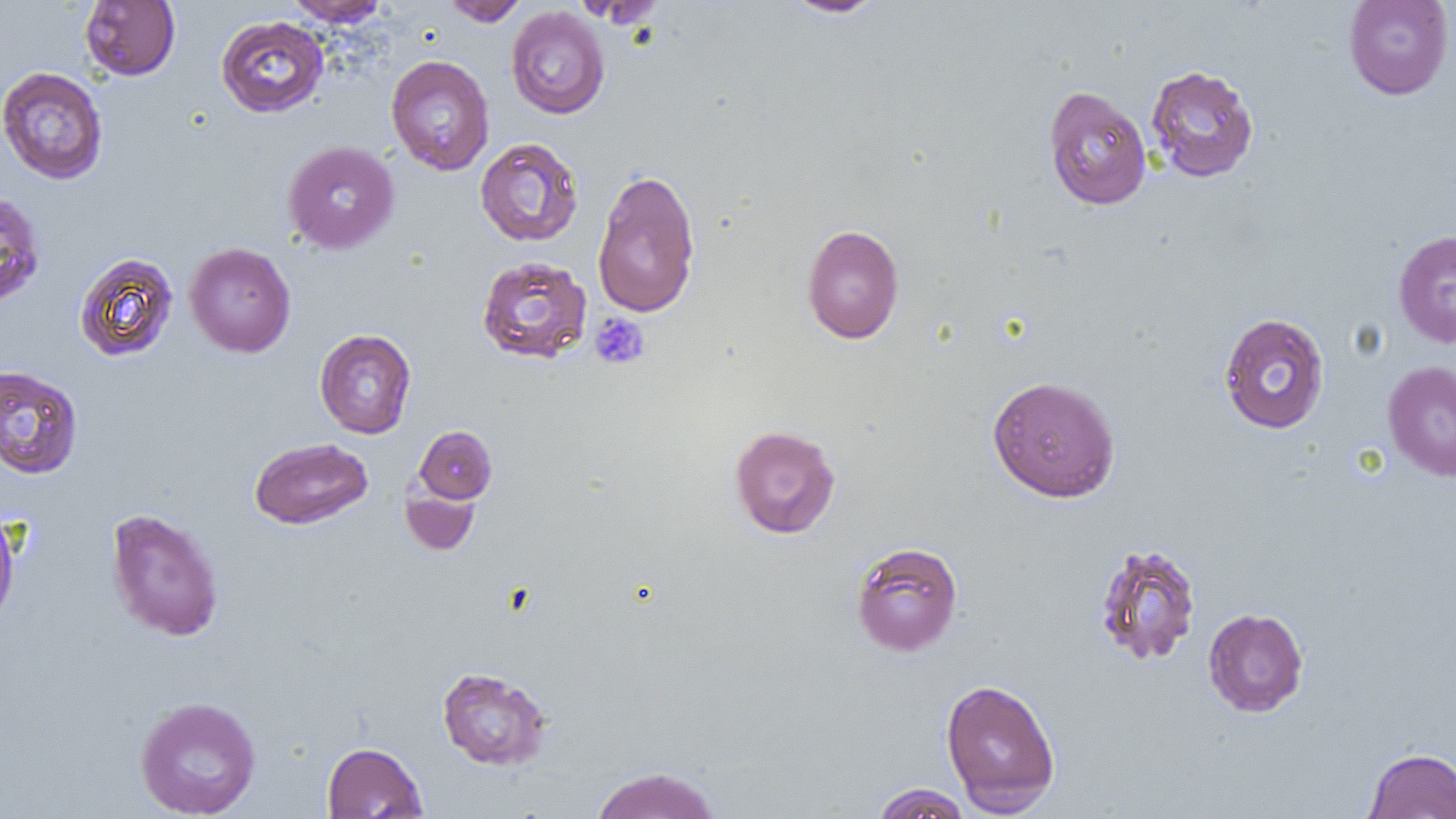

Summary:
  - Coordinate format: approximate bounding boxes as named x1/y1/x2/y2 corners in pixels
  - Uninfected red blood cell locations: (x1=284, y1=0, x2=389, y2=26), (x1=443, y1=0, x2=528, y2=26), (x1=780, y1=0, x2=888, y2=18), (x1=1343, y1=0, x2=1454, y2=100), (x1=80, y1=1, x2=180, y2=80), (x1=506, y1=6, x2=610, y2=119), (x1=216, y1=15, x2=329, y2=117), (x1=386, y1=54, x2=495, y2=175), (x1=1145, y1=64, x2=1259, y2=183), (x1=0, y1=66, x2=108, y2=184), (x1=1043, y1=85, x2=1152, y2=210), (x1=475, y1=137, x2=583, y2=247), (x1=282, y1=140, x2=399, y2=254), (x1=592, y1=168, x2=701, y2=318), (x1=0, y1=190, x2=46, y2=308), (x1=802, y1=224, x2=905, y2=344), (x1=1393, y1=229, x2=1456, y2=348), (x1=184, y1=242, x2=296, y2=357), (x1=74, y1=252, x2=179, y2=362), (x1=476, y1=256, x2=592, y2=364), (x1=1218, y1=312, x2=1330, y2=434), (x1=314, y1=329, x2=417, y2=438), (x1=1383, y1=360, x2=1456, y2=482), (x1=0, y1=364, x2=83, y2=479), (x1=987, y1=375, x2=1121, y2=503), (x1=729, y1=424, x2=841, y2=539), (x1=414, y1=425, x2=497, y2=503), (x1=250, y1=437, x2=373, y2=529), (x1=401, y1=486, x2=479, y2=556), (x1=105, y1=507, x2=225, y2=642), (x1=0, y1=512, x2=20, y2=629), (x1=850, y1=541, x2=963, y2=657), (x1=1093, y1=543, x2=1202, y2=666), (x1=1203, y1=607, x2=1309, y2=717), (x1=436, y1=666, x2=553, y2=771), (x1=940, y1=677, x2=1061, y2=814), (x1=134, y1=696, x2=261, y2=818), (x1=322, y1=742, x2=427, y2=818), (x1=1363, y1=748, x2=1456, y2=819), (x1=590, y1=766, x2=722, y2=818), (x1=871, y1=783, x2=974, y2=819)
  - Platelet locations: (x1=589, y1=313, x2=650, y2=370)
  - Slide-level diagnosis: negative for blood parasites
  - Magnification: 1000x
  - Preparation: thin blood film
  - Modality: light microscopy
  - Image size: 1456×819 pixels
  - Field of view: one of a larger specimen